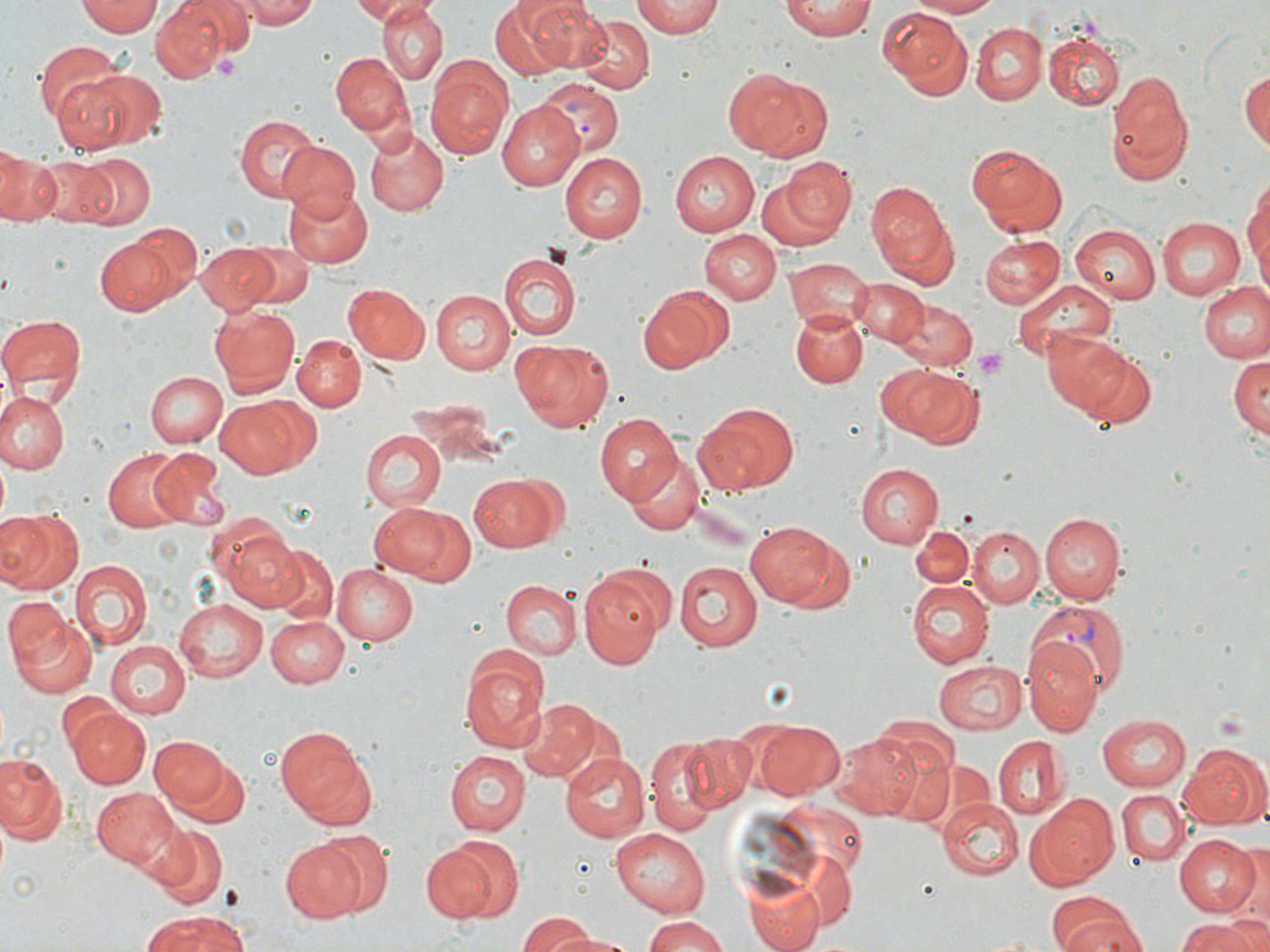

slide_level_diagnosis: Plasmodium vivax
uninfected_red_blood_cell_locations: 'approximate bounding boxes as named x1/y1/x2/y2 corners in pixels: (x1=78, y1=0, x2=163, y2=38), (x1=237, y1=0, x2=324, y2=28), (x1=348, y1=0, x2=415, y2=22), (x1=523, y1=0, x2=612, y2=72), (x1=631, y1=0, x2=726, y2=40), (x1=903, y1=0, x2=1000, y2=19), (x1=152, y1=1, x2=236, y2=78), (x1=491, y1=1, x2=580, y2=80), (x1=781, y1=1, x2=877, y2=40), (x1=376, y1=2, x2=448, y2=83), (x1=877, y1=8, x2=972, y2=98), (x1=573, y1=14, x2=652, y2=95), (x1=970, y1=22, x2=1047, y2=103), (x1=1047, y1=33, x2=1124, y2=110), (x1=34, y1=41, x2=124, y2=131), (x1=330, y1=51, x2=414, y2=138), (x1=426, y1=61, x2=511, y2=158), (x1=60, y1=67, x2=165, y2=155), (x1=724, y1=67, x2=831, y2=162), (x1=1240, y1=67, x2=1269, y2=155), (x1=1105, y1=71, x2=1195, y2=187), (x1=496, y1=103, x2=582, y2=190), (x1=232, y1=114, x2=320, y2=201), (x1=362, y1=127, x2=448, y2=217), (x1=279, y1=142, x2=361, y2=216), (x1=967, y1=144, x2=1066, y2=234), (x1=1, y1=151, x2=55, y2=224), (x1=561, y1=151, x2=651, y2=243), (x1=670, y1=152, x2=759, y2=236), (x1=32, y1=153, x2=126, y2=225), (x1=70, y1=153, x2=153, y2=228), (x1=777, y1=155, x2=857, y2=239), (x1=1243, y1=178, x2=1270, y2=287), (x1=867, y1=179, x2=956, y2=286), (x1=281, y1=186, x2=373, y2=268), (x1=1155, y1=217, x2=1244, y2=301), (x1=134, y1=223, x2=203, y2=302), (x1=1069, y1=224, x2=1159, y2=305), (x1=698, y1=229, x2=781, y2=304), (x1=979, y1=234, x2=1065, y2=310), (x1=94, y1=236, x2=180, y2=317), (x1=197, y1=244, x2=280, y2=310), (x1=240, y1=244, x2=313, y2=307), (x1=500, y1=252, x2=581, y2=339), (x1=784, y1=256, x2=872, y2=327), (x1=797, y1=264, x2=930, y2=339), (x1=851, y1=278, x2=926, y2=347), (x1=1012, y1=279, x2=1117, y2=363), (x1=1199, y1=281, x2=1270, y2=364), (x1=343, y1=283, x2=432, y2=365), (x1=638, y1=284, x2=736, y2=374), (x1=431, y1=289, x2=515, y2=374), (x1=888, y1=297, x2=978, y2=373), (x1=208, y1=305, x2=300, y2=397), (x1=791, y1=310, x2=868, y2=387), (x1=0, y1=315, x2=85, y2=403), (x1=1041, y1=330, x2=1132, y2=415), (x1=292, y1=334, x2=364, y2=412), (x1=512, y1=338, x2=616, y2=432), (x1=1072, y1=351, x2=1158, y2=430), (x1=1228, y1=352, x2=1270, y2=439), (x1=877, y1=363, x2=980, y2=446), (x1=144, y1=370, x2=226, y2=448), (x1=0, y1=391, x2=66, y2=474), (x1=215, y1=398, x2=308, y2=478), (x1=698, y1=403, x2=800, y2=493), (x1=594, y1=411, x2=681, y2=502), (x1=361, y1=429, x2=447, y2=514), (x1=150, y1=446, x2=228, y2=525), (x1=105, y1=448, x2=189, y2=527), (x1=623, y1=457, x2=704, y2=537), (x1=854, y1=464, x2=944, y2=549), (x1=469, y1=473, x2=562, y2=552), (x1=368, y1=501, x2=461, y2=582), (x1=0, y1=511, x2=79, y2=594), (x1=1039, y1=514, x2=1127, y2=606), (x1=744, y1=518, x2=847, y2=612), (x1=217, y1=525, x2=305, y2=611), (x1=968, y1=525, x2=1044, y2=608), (x1=911, y1=526, x2=973, y2=589), (x1=272, y1=547, x2=338, y2=624), (x1=674, y1=559, x2=763, y2=652), (x1=70, y1=560, x2=151, y2=650), (x1=331, y1=562, x2=418, y2=645), (x1=578, y1=565, x2=671, y2=668), (x1=500, y1=579, x2=581, y2=660), (x1=907, y1=580, x2=992, y2=668), (x1=3, y1=596, x2=74, y2=672), (x1=174, y1=596, x2=270, y2=682), (x1=267, y1=614, x2=350, y2=687), (x1=8, y1=616, x2=99, y2=699), (x1=1024, y1=640, x2=1103, y2=737), (x1=106, y1=641, x2=191, y2=718), (x1=457, y1=647, x2=550, y2=755), (x1=932, y1=658, x2=1026, y2=735), (x1=521, y1=698, x2=599, y2=779), (x1=67, y1=707, x2=149, y2=789), (x1=1096, y1=713, x2=1191, y2=792), (x1=754, y1=719, x2=846, y2=799), (x1=276, y1=722, x2=374, y2=826), (x1=836, y1=730, x2=926, y2=820), (x1=680, y1=732, x2=759, y2=813), (x1=992, y1=735, x2=1069, y2=819), (x1=151, y1=736, x2=229, y2=811), (x1=646, y1=738, x2=723, y2=833), (x1=1180, y1=743, x2=1268, y2=831), (x1=881, y1=746, x2=965, y2=827), (x1=169, y1=750, x2=251, y2=831), (x1=444, y1=751, x2=530, y2=836), (x1=561, y1=753, x2=647, y2=841), (x1=0, y1=755, x2=67, y2=846), (x1=91, y1=787, x2=177, y2=866), (x1=1117, y1=787, x2=1191, y2=867), (x1=1029, y1=793, x2=1119, y2=887), (x1=936, y1=797, x2=1021, y2=882), (x1=609, y1=824, x2=711, y2=913), (x1=149, y1=827, x2=229, y2=908), (x1=310, y1=833, x2=392, y2=914), (x1=1172, y1=834, x2=1263, y2=918), (x1=422, y1=839, x2=511, y2=923), (x1=280, y1=840, x2=368, y2=923), (x1=1233, y1=849, x2=1270, y2=934), (x1=744, y1=875, x2=825, y2=952), (x1=1054, y1=901, x2=1148, y2=952), (x1=137, y1=913, x2=254, y2=952), (x1=518, y1=914, x2=597, y2=949), (x1=1179, y1=915, x2=1268, y2=952), (x1=641, y1=916, x2=732, y2=951), (x1=537, y1=926, x2=632, y2=951)'
field_of_view: one of a larger specimen
stain: May-Grünwald-Giemsa
modality: optical microscopy
magnification: 1000x
platelet_locations: 'approximate bounding boxes as named x1/y1/x2/y2 corners in pixels: (x1=215, y1=54, x2=241, y2=79), (x1=971, y1=347, x2=1010, y2=382)'
plasmodium_vivax_infected_red_blood_cell_locations: 'approximate bounding boxes as named x1/y1/x2/y2 corners in pixels: (x1=540, y1=81, x2=623, y2=158), (x1=1028, y1=601, x2=1132, y2=693)'
preparation: thin blood smear
image_size: 1270×952 pixels